Identify the blood parasite species.
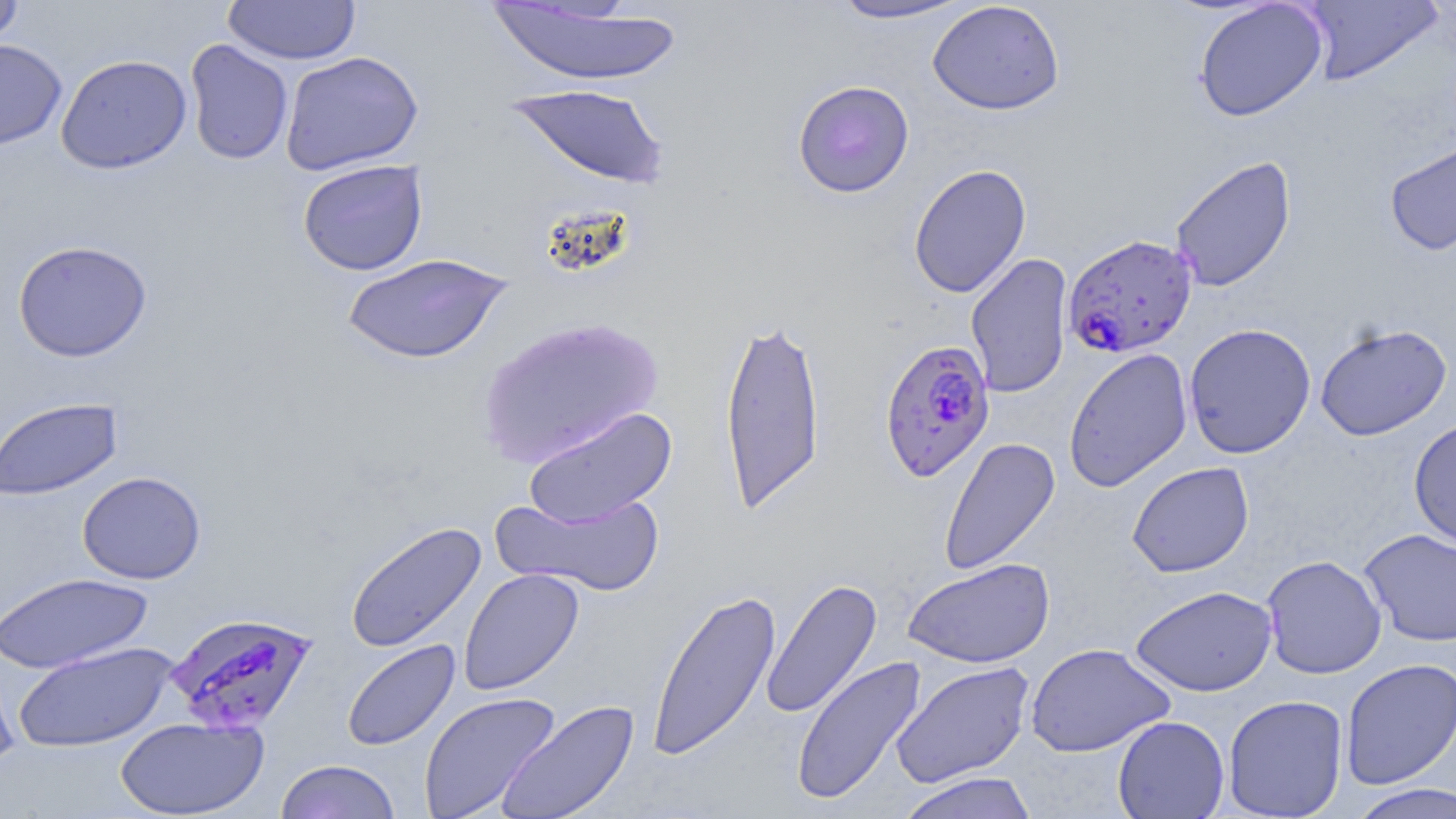
Plasmodium falciparum.

Approximate bounding boxes as [x1, y1, x2, y2] in pixels. Uninfected red blood cell locations: [0, 0, 24, 51], [829, 0, 974, 24], [1299, 0, 1444, 85], [222, 1, 361, 65], [927, 1, 1065, 115], [1193, 1, 1328, 122], [486, 4, 682, 86], [0, 38, 67, 151], [184, 39, 294, 165], [279, 51, 423, 176], [56, 54, 192, 174], [792, 79, 915, 198], [504, 84, 671, 189], [1384, 136, 1456, 256], [1170, 155, 1296, 292], [297, 159, 429, 276], [909, 163, 1032, 298], [13, 240, 152, 362], [966, 253, 1074, 398], [341, 254, 512, 365], [719, 313, 826, 515], [475, 315, 664, 468], [1314, 322, 1452, 441], [1184, 323, 1316, 459], [1064, 348, 1193, 491], [0, 397, 124, 501], [522, 406, 677, 528], [1408, 417, 1456, 553], [938, 436, 1060, 575], [1127, 461, 1254, 578], [77, 471, 206, 584], [492, 490, 666, 597], [344, 521, 487, 654], [1359, 528, 1456, 646], [1261, 554, 1387, 679], [902, 558, 1055, 668], [458, 568, 584, 696], [1, 571, 154, 674], [760, 578, 883, 719], [1130, 585, 1278, 696], [646, 587, 782, 761], [341, 639, 460, 752], [12, 641, 178, 753], [1026, 643, 1175, 757], [0, 647, 21, 772], [791, 655, 928, 807], [1339, 659, 1456, 790], [890, 660, 1035, 789], [418, 691, 560, 819], [1223, 694, 1348, 818], [495, 698, 641, 819], [1112, 715, 1230, 818], [115, 716, 269, 818], [275, 759, 400, 819], [895, 771, 1039, 819], [1344, 782, 1456, 819]. Plasmodium falciparum-infected red blood cell locations: [1063, 233, 1198, 358], [878, 338, 995, 482], [166, 611, 319, 735]. Light microscopy. May-Grünwald-Giemsa-stained preparation. Captured at 1000x magnification. One field of a larger specimen. Image is 1456×819 pixels. Thin blood film.